Assess this cell for malaria.
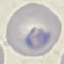
Parasitized.

capture: smartphone through the microscope eyepiece
preparation: thin smear
stain: Giemsa
image_type: cell patch, automatically extracted from a larger field of view and resized to 64 × 64 pixels